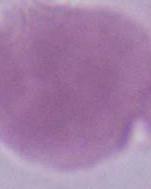

identification = red blood cell
modality = micrograph
magnification = 1000x